Report the malaria status of this cell.
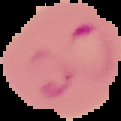
It is parasitized.

Summary:
  - Image type: cell region segmented out of the field of view; surrounding area masked to black
  - Preparation: thin blood film
  - Image size: 121×121 pixels